Assess this cell for malaria.
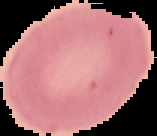
Uninfected.

Image is 157×136 pixels. The area outside the segmented cell region is set to black. From a thin blood film.